State which parasite is depicted.
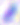
Toxoplasma gondii.

modality = photomicrograph
magnification = 400x